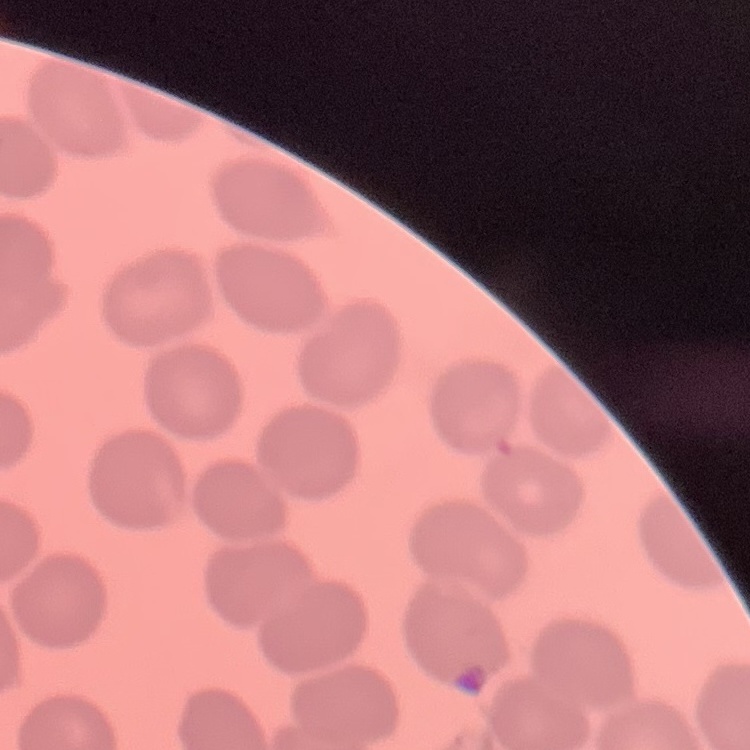
The erythrocytes exhibit no rouleaux formation. Thin peripheral smear. Stained with either Field's or Giemsa. Square crop of a larger photomicrograph.